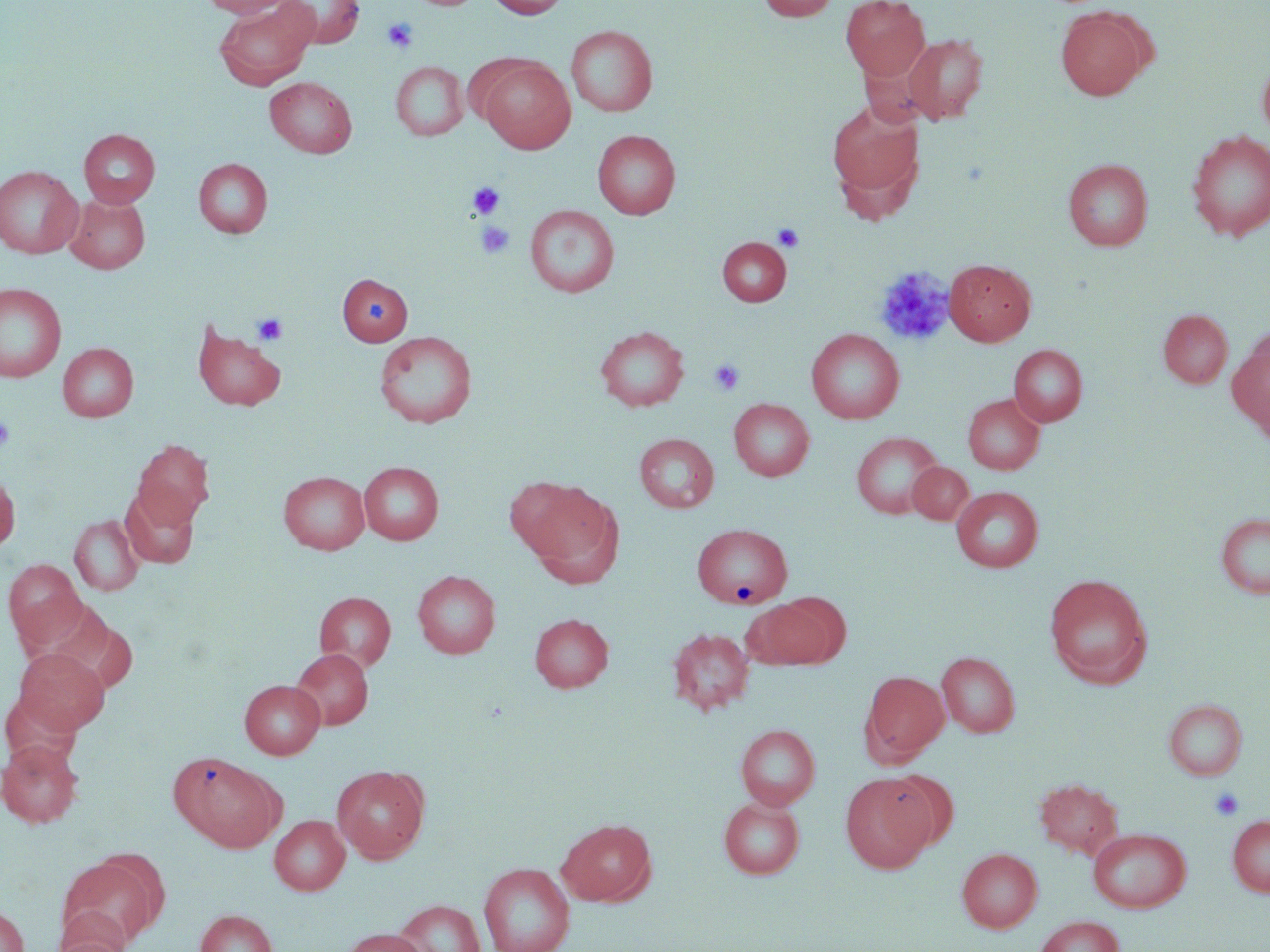
slide_level_diagnosis: no evidence of blood parasites
uninfected_red_blood_cell_locations: 'approximate bounding boxes as (x1,y1)-(x2,y2) corner pairs in pixels: (199,0)-(295,18), (276,0)-(364,48), (411,0)-(483,10), (487,0)-(569,18), (757,0)-(840,21), (841,0)-(930,80), (214,2)-(320,90), (1055,7)-(1151,100), (566,25)-(658,116), (902,33)-(988,125), (477,57)-(575,153), (1257,57)-(1270,142), (391,62)-(468,141), (265,77)-(357,158), (827,99)-(925,214), (78,129)-(160,208), (592,130)-(680,219), (1185,130)-(1270,241), (194,158)-(272,238), (1063,159)-(1153,251), (0,165)-(83,259), (65,193)-(150,274), (525,205)-(619,297), (718,237)-(792,306), (944,259)-(1036,345), (338,273)-(413,345), (0,282)-(66,382), (1158,309)-(1233,388), (192,321)-(286,410), (595,326)-(688,411), (806,328)-(904,424), (374,331)-(478,428), (1227,333)-(1270,436), (58,343)-(138,421), (1009,344)-(1087,427), (962,394)-(1045,474), (729,398)-(814,481), (851,432)-(943,519), (635,433)-(718,512), (132,439)-(215,526), (359,462)-(443,544), (907,462)-(973,524), (0,471)-(20,554), (278,471)-(370,554), (516,480)-(621,581), (120,485)-(199,568), (952,486)-(1044,572), (1215,513)-(1270,598), (70,514)-(144,596), (695,525)-(797,612), (3,559)-(86,648), (412,570)-(500,659), (1044,573)-(1153,687), (314,591)-(396,671), (756,595)-(844,669), (530,613)-(614,692), (667,627)-(755,715), (14,648)-(110,735), (290,648)-(373,730), (937,651)-(1020,738), (862,671)-(949,762), (239,679)-(325,759), (1163,698)-(1247,781), (735,724)-(820,810), (0,739)-(84,829), (169,751)-(281,852), (332,765)-(429,863), (881,769)-(958,851), (840,774)-(934,872), (1034,777)-(1124,860), (719,797)-(805,879), (270,815)-(350,895), (1228,815)-(1270,897), (557,817)-(657,907), (1088,828)-(1191,912), (957,848)-(1042,932), (57,853)-(165,949), (479,863)-(575,952), (394,899)-(486,951), (0,905)-(30,952), (195,910)-(278,952), (1034,915)-(1124,952), (339,928)-(429,952), (50,931)-(130,952)'
platelet_locations: 'approximate bounding boxes as (x1,y1)-(x2,y2) corner pairs in pixels: (382,17)-(418,53), (468,182)-(504,219), (476,221)-(514,259), (772,223)-(804,252), (874,267)-(955,347), (253,313)-(288,345), (709,359)-(745,395), (0,416)-(16,450), (1209,787)-(1244,820)'
magnification: 1000x
field_of_view: single
image_size: 1270×952 pixels
modality: light microscopy
preparation: thin blood smear
stain: May-Grünwald-Giemsa